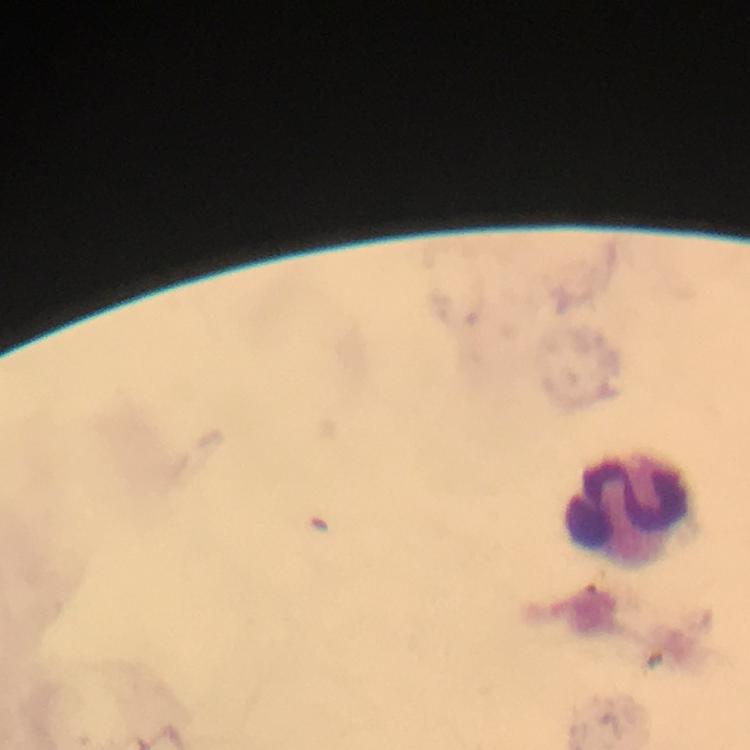

Approximate centers as {x, y} in pixels.
Summary:
  - Leukocyte locations: {632, 509}
  - Malaria parasites: none seen
  - Magnification: 100x
  - Preparation: thick smear
  - Immersion oil: applied
  - Image size: 750×750 pixels
  - Stain: Giemsa
  - Cropped from: one field of view
  - Context: from a diagnostic examination for malaria
  - Capture: smartphone camera through the microscope